Comment on the morphology of the erythrocytes.
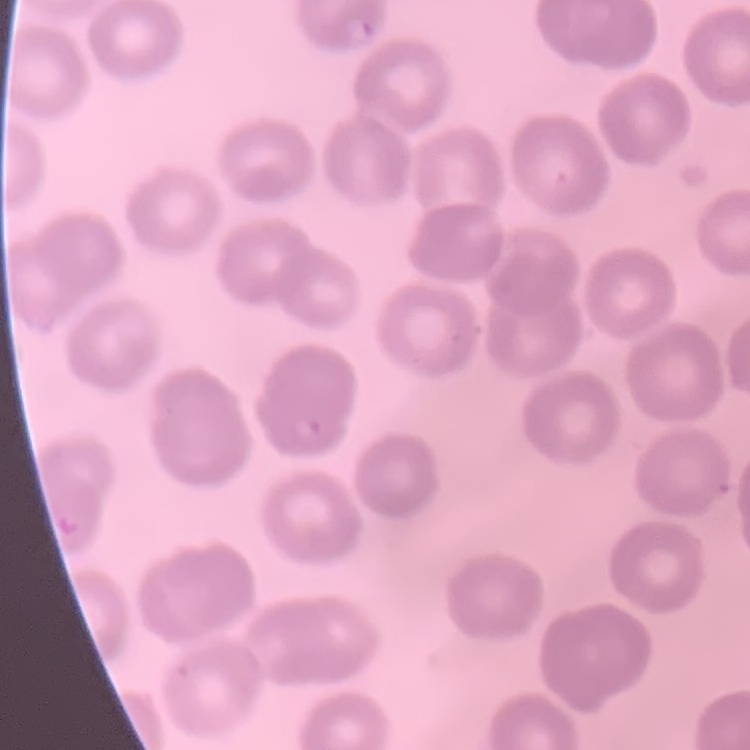

No rouleaux formation.

Summary:
  - Stain: Field's or Giemsa
  - Preparation: thin peripheral smear
  - Image type: one tile cut from a larger photomicrograph